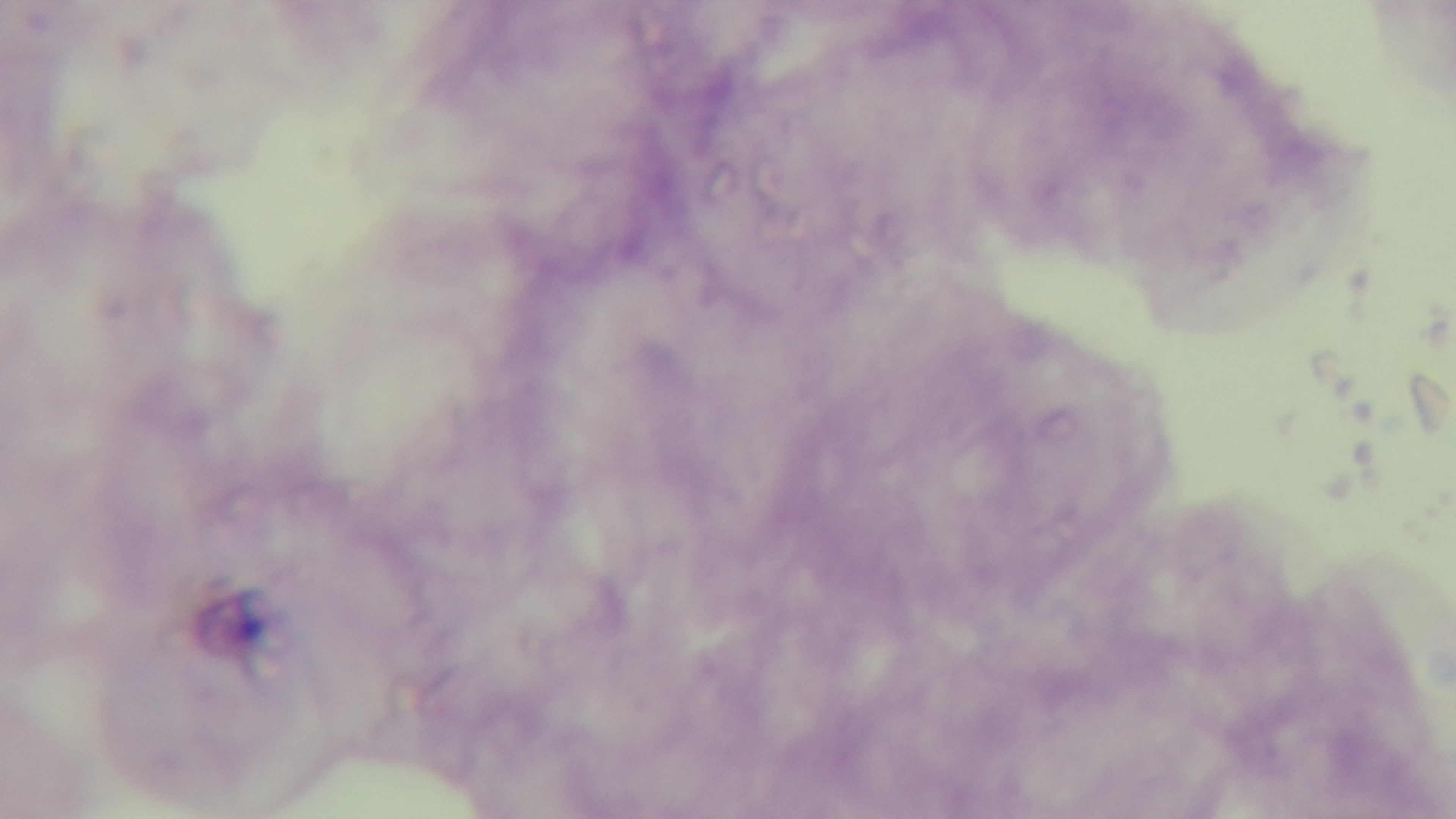

{
  "objective": "100x oil immersion",
  "modality": "light microscopy",
  "stain": "Giemsa",
  "preparation": "thick",
  "malaria_status": "negative",
  "field_of_view": "one from the slide",
  "capture": "mounted 4K digital camera"
}